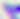 Micrograph. Toxoplasma gondii is shown. Captured at 400x magnification.